Locate and identify every blood parasite.
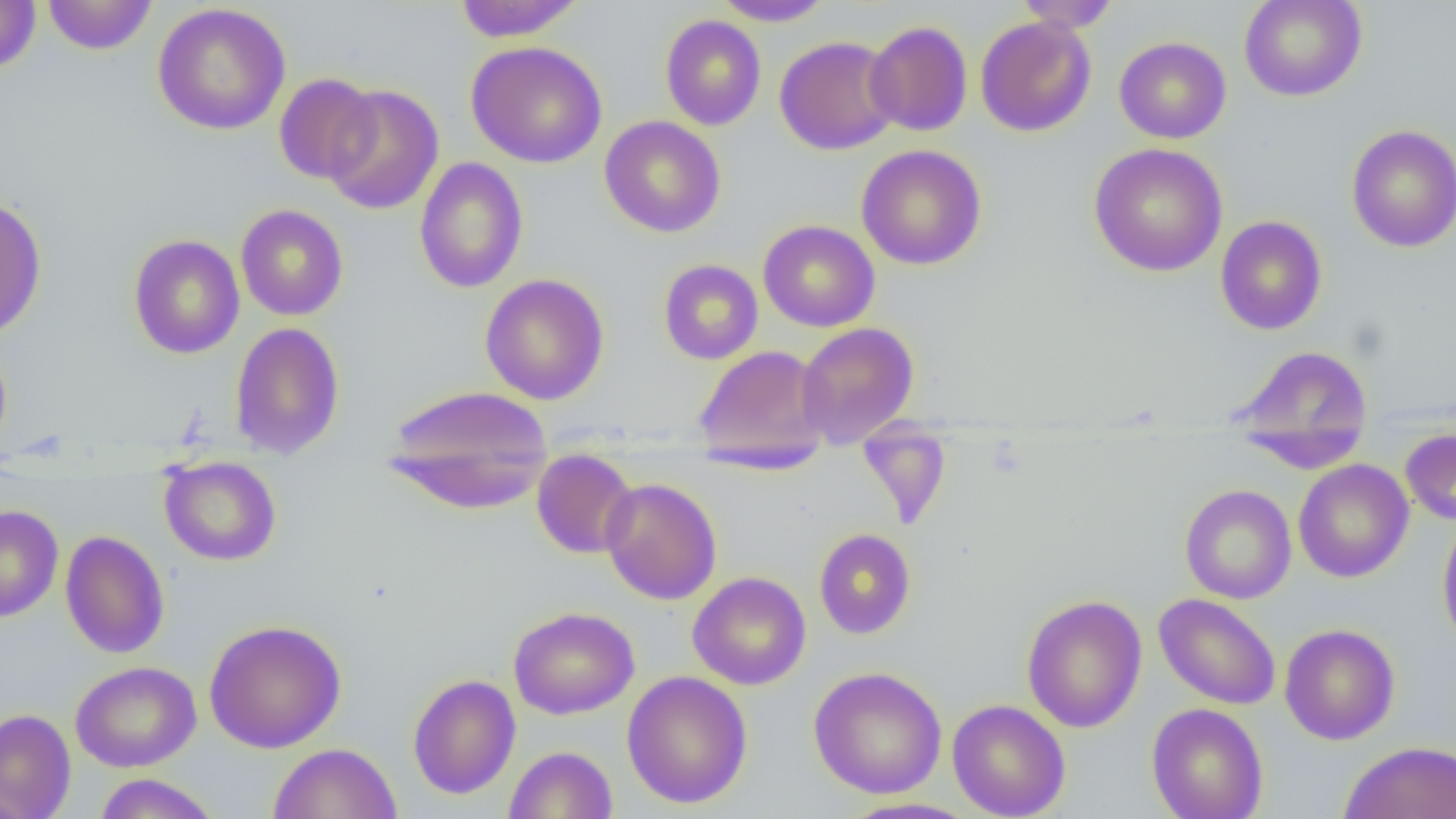
No blood parasites seen.

Approximate bounding boxes as (x1, y1, x2, y2) in pixels. Uninfected red blood cell locations: (42, 0, 157, 55), (453, 0, 586, 42), (711, 0, 836, 26), (1014, 0, 1121, 32), (1239, 0, 1368, 102), (0, 1, 40, 74), (151, 3, 291, 135), (660, 15, 766, 131), (975, 16, 1096, 137), (865, 20, 973, 136), (774, 35, 901, 155), (1114, 36, 1231, 143), (466, 41, 608, 168), (274, 73, 381, 184), (322, 84, 444, 215), (599, 115, 727, 238), (1346, 124, 1456, 252), (1089, 142, 1228, 277), (857, 144, 986, 270), (414, 157, 528, 293), (0, 195, 47, 341), (236, 204, 348, 321), (1215, 215, 1327, 335), (758, 219, 880, 332), (128, 234, 245, 359), (658, 259, 763, 364), (480, 273, 609, 405), (229, 321, 345, 460), (796, 322, 919, 448), (0, 341, 12, 458), (1231, 343, 1373, 465), (694, 345, 831, 464), (382, 384, 554, 514), (856, 419, 951, 529), (1400, 428, 1456, 525), (531, 449, 638, 559), (159, 456, 282, 566), (1293, 459, 1414, 583), (600, 477, 722, 605), (1179, 484, 1296, 604), (0, 504, 64, 623), (1437, 513, 1456, 652), (814, 528, 916, 639), (60, 530, 169, 659), (687, 572, 811, 690), (1154, 593, 1282, 710), (1021, 594, 1147, 732), (508, 606, 639, 719), (204, 619, 346, 753), (1279, 623, 1400, 745), (70, 660, 201, 772), (808, 666, 947, 799), (622, 670, 753, 809), (407, 673, 520, 799), (947, 699, 1070, 819), (1147, 703, 1268, 819), (0, 708, 76, 819), (1340, 741, 1456, 819), (268, 743, 402, 818), (505, 745, 618, 819), (93, 773, 221, 818), (837, 798, 980, 819). Slide-level diagnosis: no evidence of blood parasites. Image is 1456×819 pixels. 1000x magnification. Optical microscopy. Thin blood film. Single field of view.